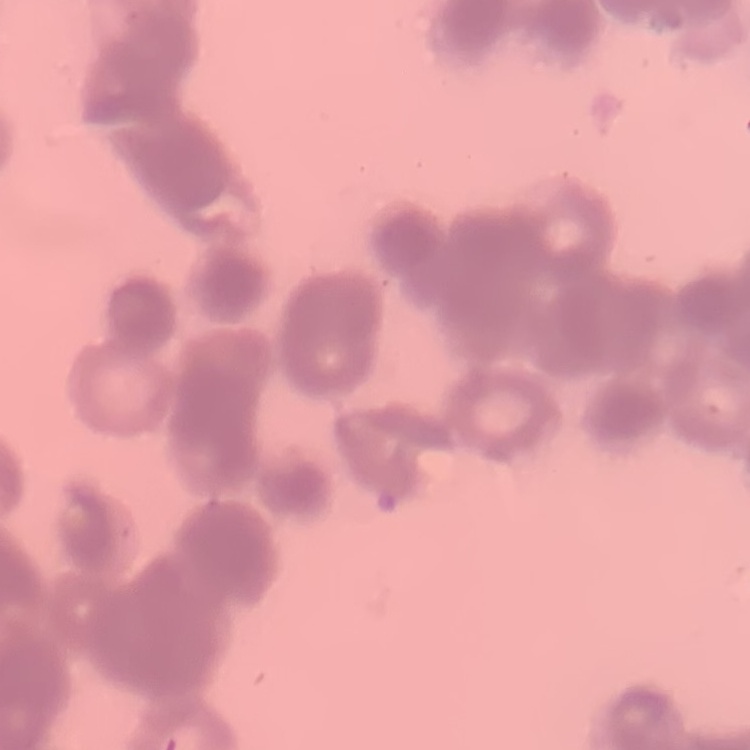
The red blood cells show rouleaux formation. Stained with either Field's or Giemsa. Thin blood film. One tile cut from a larger photomicrograph.